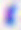
identification = Toxoplasma gondii
magnification = 400x
modality = micrograph